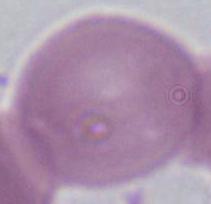 An erythrocyte is seen. Photomicrograph. Captured at 1000x magnification.